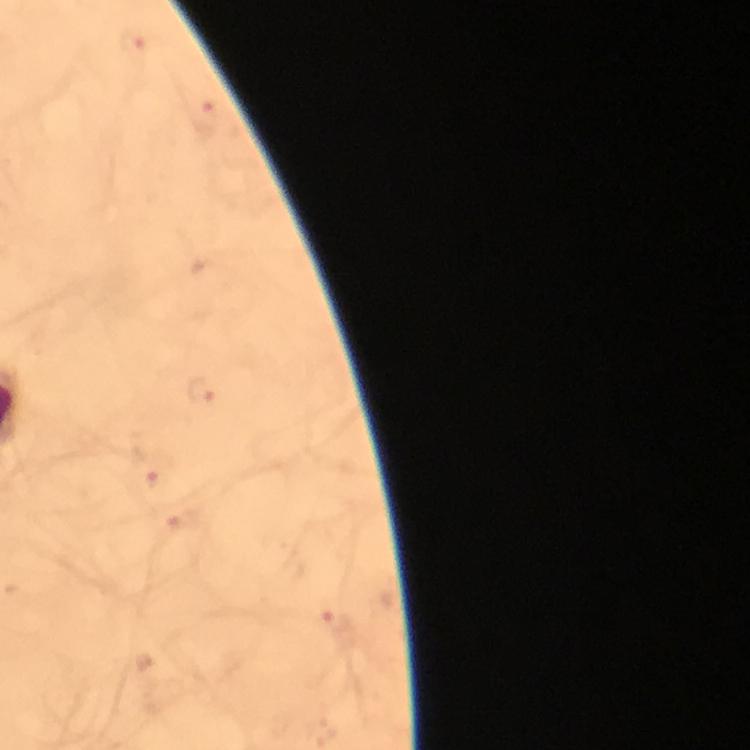
preparation: thick blood film
magnification: 100x
image_size: 750×750 pixels
stain: Giemsa
cropped_from: a single field of view
immersion_oil: used
capture: smartphone mounted on the microscope
plasmodium_parasite_locations: 'approximate centers as [x, y] in pixels: [133, 45], [207, 117], [205, 390], [152, 472], [337, 624]'
context: from a diagnostic examination for malaria